Name the parasite shown.
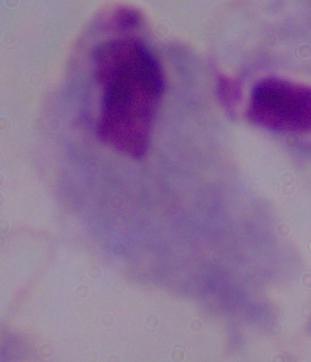

This is a trichomonad.

magnification: 1000x
modality: photomicrograph